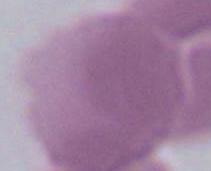

Summary:
  - Magnification: 1000x
  - Identification: erythrocyte
  - Modality: micrograph